Name the parasite shown.
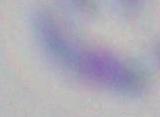
Toxoplasma gondii.

Captured at 1000x magnification. Photomicrograph.